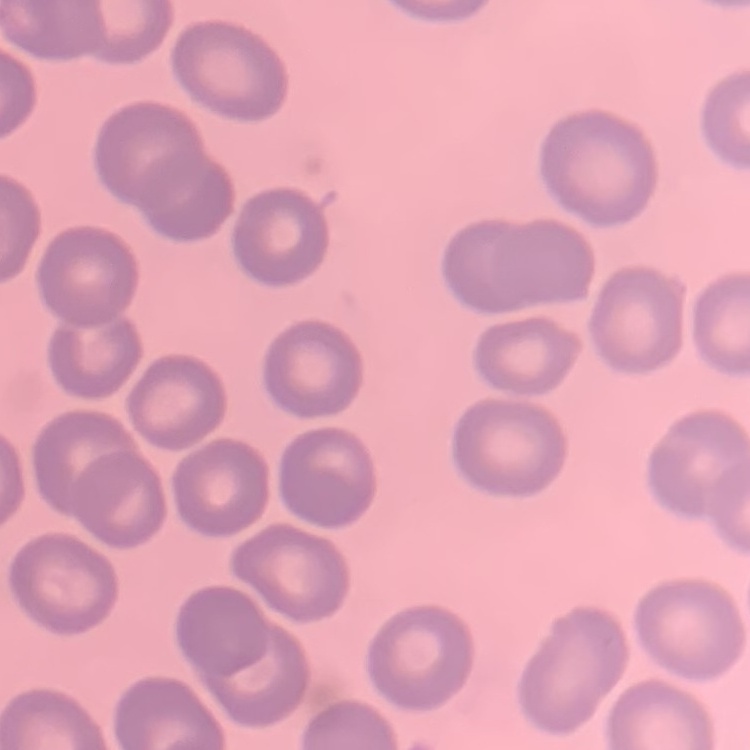

Summary:
  - Red blood cell morphology: no rouleaux formation
  - Stain: Field's or Giemsa
  - Image type: square crop of a larger photomicrograph
  - Preparation: thin blood smear